Name the parasite shown.
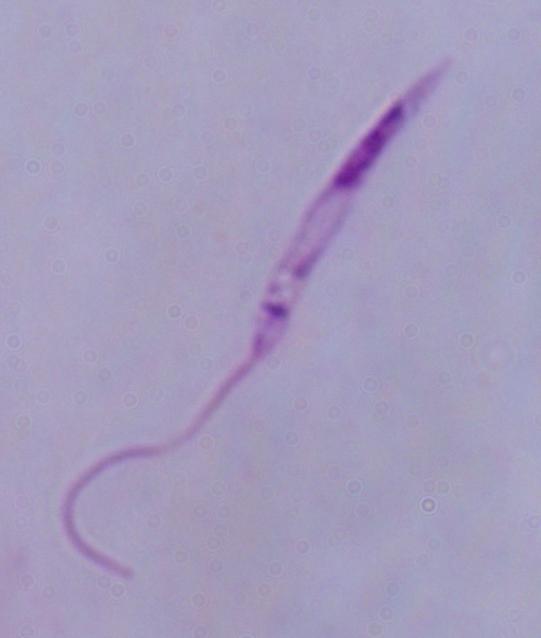

Leishmania.

Captured at 1000x magnification. Micrograph.